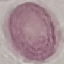

Summary:
  - Malaria status: uninfected
  - Capture: smartphone camera at the microscope eyepiece
  - Image type: cell patch, automatically extracted from a larger field of view and resized to 64 × 64 pixels
  - Stain: Giemsa
  - Preparation: thin blood film